Comment on the morphology of the red blood cells.
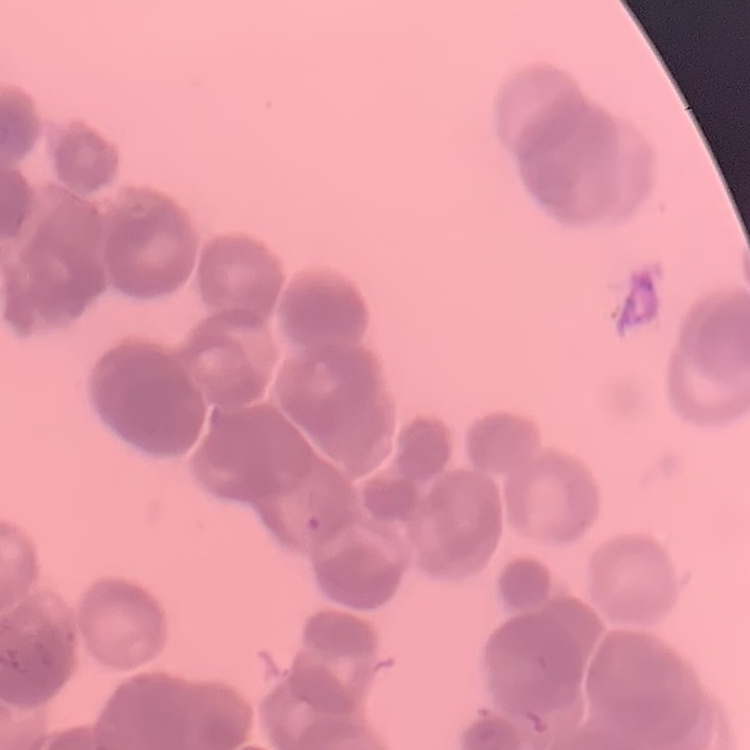

They show rouleaux formation.

preparation = thin blood film
stain = Field's or Giemsa
image type = square crop of a larger photomicrograph